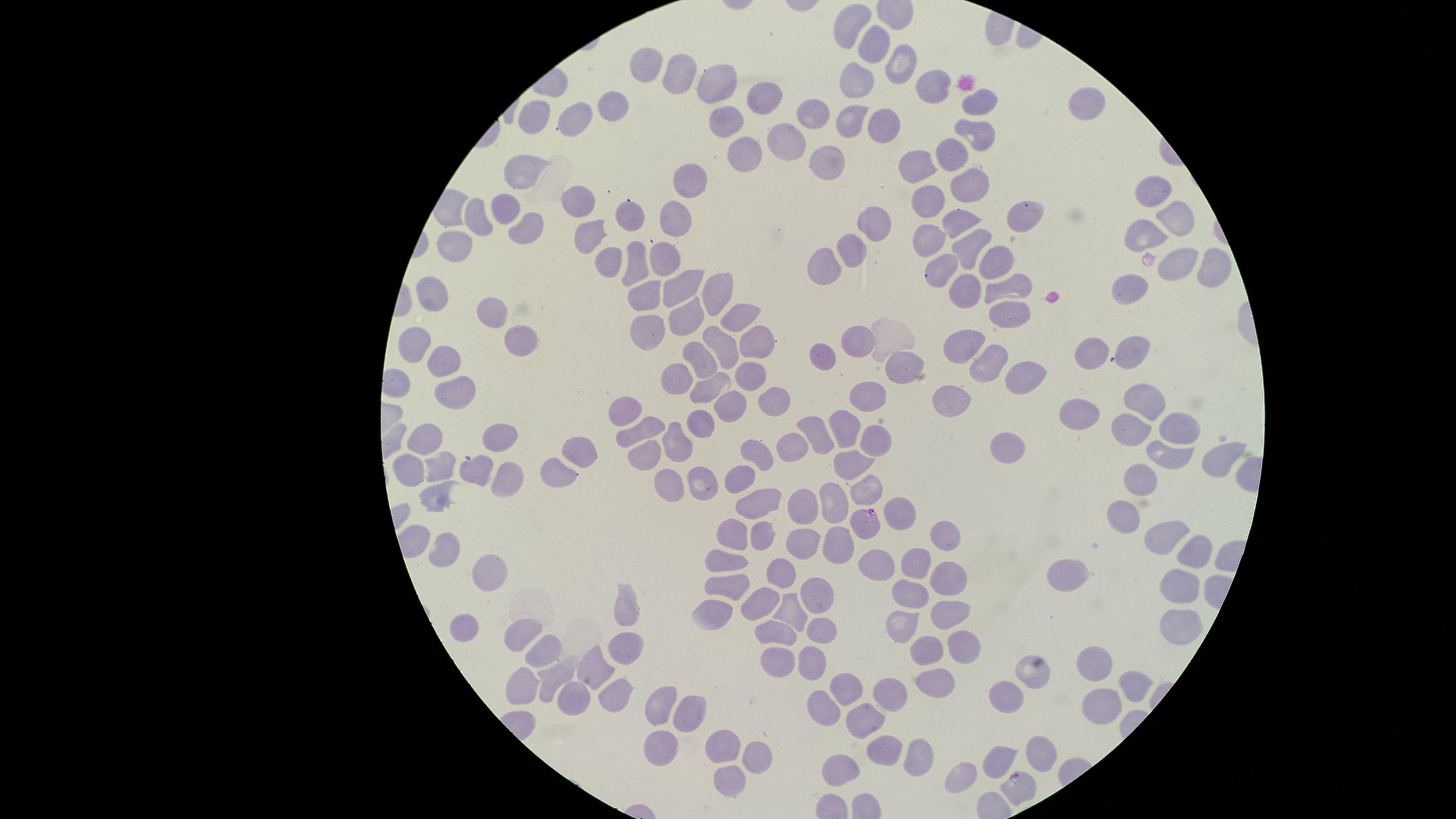
{
  "image_size": "1456×819 pixels",
  "presence": "malaria parasites detected",
  "parasitized_red_blood_cells": "approximate marker points, in pixels from the top-left corner: (x=1026, y=210), (x=935, y=272), (x=868, y=525), (x=1018, y=783)",
  "capture": "smartphone photograph through the microscope eyepiece",
  "preparation": "thin blood smear",
  "field_of_view": "single",
  "stain": "Giemsa",
  "visible_region": "circular",
  "species": "Plasmodium falciparum",
  "uninfected_red_blood_cells": "approximate marker points, in pixels from the top-left corner: (x=854, y=22), (x=873, y=43), (x=901, y=59), (x=649, y=64), (x=676, y=67), (x=857, y=77), (x=721, y=78), (x=932, y=87), (x=763, y=89), (x=616, y=99), (x=978, y=102), (x=1084, y=104), (x=814, y=114), (x=856, y=114), (x=541, y=116), (x=584, y=116), (x=725, y=121), (x=885, y=129), (x=980, y=130), (x=787, y=139), (x=953, y=149), (x=744, y=151), (x=834, y=154), (x=918, y=163), (x=521, y=168), (x=691, y=181), (x=965, y=183), (x=1151, y=192), (x=930, y=200), (x=579, y=201), (x=510, y=208), (x=632, y=215), (x=476, y=217), (x=678, y=218), (x=960, y=218), (x=1170, y=219), (x=875, y=223), (x=1140, y=225), (x=530, y=227), (x=592, y=234), (x=930, y=237), (x=456, y=244), (x=850, y=244), (x=966, y=245), (x=667, y=255), (x=993, y=258), (x=606, y=260), (x=830, y=261), (x=633, y=262), (x=1203, y=264), (x=1176, y=270), (x=677, y=284), (x=711, y=287), (x=998, y=287), (x=1131, y=287), (x=970, y=288), (x=440, y=291), (x=640, y=294), (x=489, y=309), (x=1011, y=310), (x=685, y=316), (x=734, y=321), (x=642, y=330), (x=526, y=341), (x=860, y=342), (x=969, y=344), (x=413, y=345), (x=1135, y=345), (x=755, y=346), (x=722, y=348), (x=816, y=352), (x=704, y=354), (x=1089, y=354), (x=438, y=359), (x=981, y=362), (x=914, y=366), (x=679, y=372), (x=746, y=374), (x=1015, y=374), (x=711, y=384), (x=462, y=392), (x=1139, y=397), (x=868, y=398), (x=955, y=398), (x=773, y=399), (x=729, y=405), (x=628, y=408), (x=1074, y=412), (x=707, y=421), (x=813, y=423), (x=842, y=423), (x=1177, y=427), (x=642, y=428), (x=1125, y=429), (x=428, y=437), (x=500, y=437), (x=675, y=438), (x=880, y=439), (x=1009, y=444), (x=788, y=446), (x=582, y=454), (x=754, y=456), (x=1171, y=458), (x=643, y=460), (x=1224, y=461), (x=442, y=466), (x=558, y=467), (x=851, y=467), (x=412, y=468), (x=479, y=472), (x=706, y=476), (x=514, y=478), (x=1139, y=480), (x=664, y=483), (x=738, y=483), (x=871, y=489), (x=443, y=496), (x=757, y=504), (x=803, y=504), (x=827, y=505), (x=898, y=508), (x=1125, y=518), (x=941, y=533), (x=763, y=535), (x=734, y=536), (x=1164, y=540), (x=801, y=543), (x=836, y=543), (x=445, y=549), (x=1194, y=554), (x=725, y=559), (x=909, y=560), (x=875, y=564), (x=483, y=569), (x=951, y=572), (x=1067, y=574), (x=774, y=575), (x=731, y=590), (x=819, y=590), (x=910, y=590), (x=1179, y=590), (x=755, y=601), (x=946, y=605), (x=629, y=608), (x=785, y=611), (x=714, y=614), (x=903, y=620), (x=467, y=624), (x=1179, y=624), (x=821, y=630), (x=769, y=632), (x=523, y=635), (x=542, y=650), (x=628, y=650), (x=935, y=650), (x=959, y=650), (x=1092, y=655), (x=808, y=658), (x=779, y=660), (x=601, y=666), (x=557, y=674), (x=1028, y=675), (x=1132, y=680), (x=934, y=683), (x=836, y=687), (x=530, y=690), (x=617, y=695), (x=575, y=698), (x=885, y=702), (x=1004, y=702), (x=1101, y=704), (x=659, y=708), (x=823, y=708), (x=686, y=710), (x=866, y=721), (x=725, y=742), (x=659, y=752), (x=887, y=752), (x=917, y=755), (x=755, y=756), (x=1044, y=757), (x=997, y=762), (x=846, y=763), (x=727, y=776), (x=965, y=776)"
}